Point out each Plasmodium parasite.
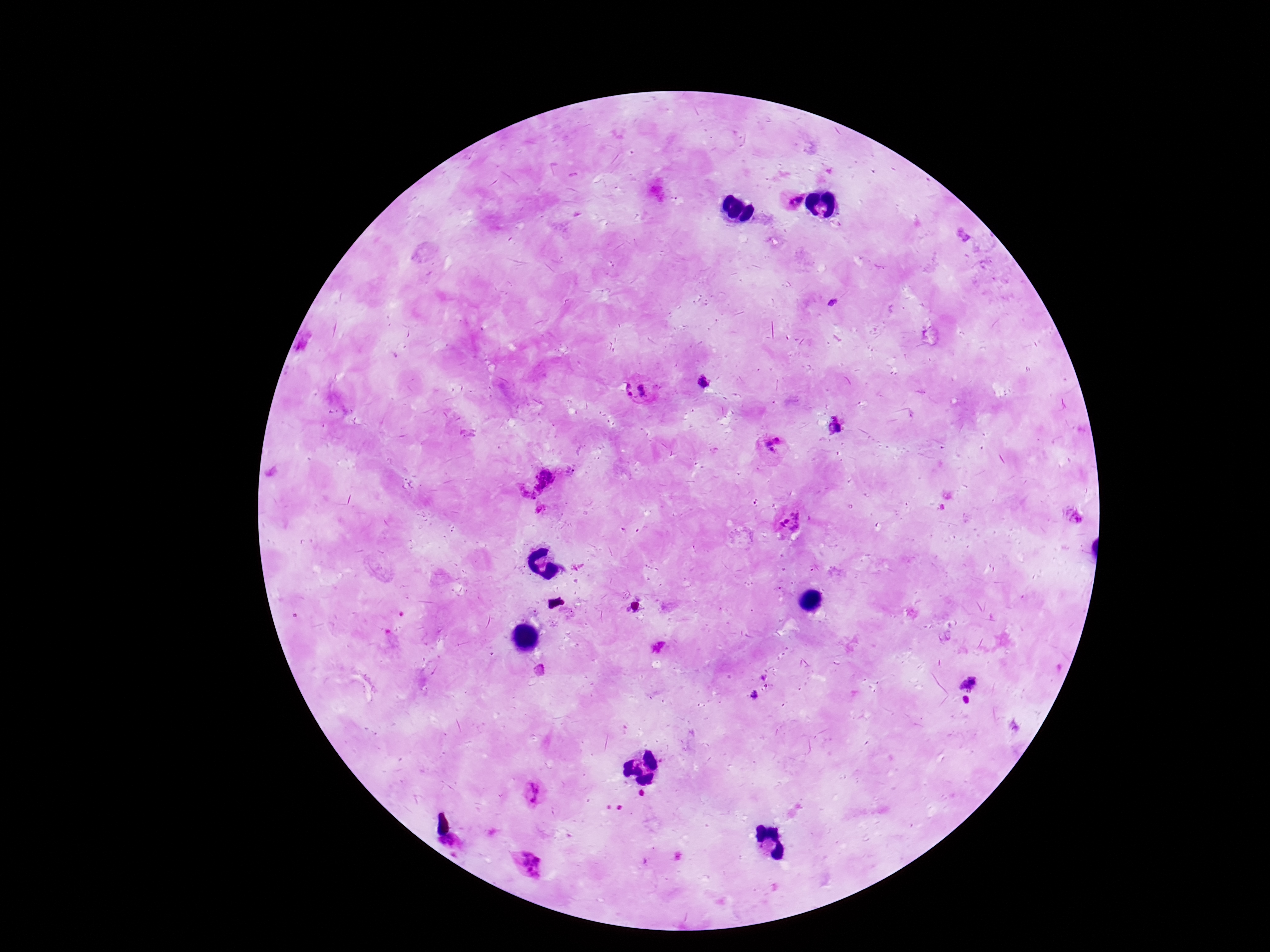

Approximate centers as (x, y) in pixels.
Plasmodium parasites: (794, 198), (704, 382), (639, 390), (837, 428), (774, 445), (570, 469), (533, 480), (542, 512), (1080, 518), (793, 521), (658, 646), (540, 670), (969, 683), (754, 694), (533, 794), (453, 841), (528, 863).

Summary:
  - Patient malaria status: infected
  - Field of view: single
  - Image size: 1270×952 pixels
  - Magnification: 100x
  - Stain: Giemsa
  - Preparation: thick peripheral-blood smear
  - Capture: smartphone camera through the microscope eyepiece